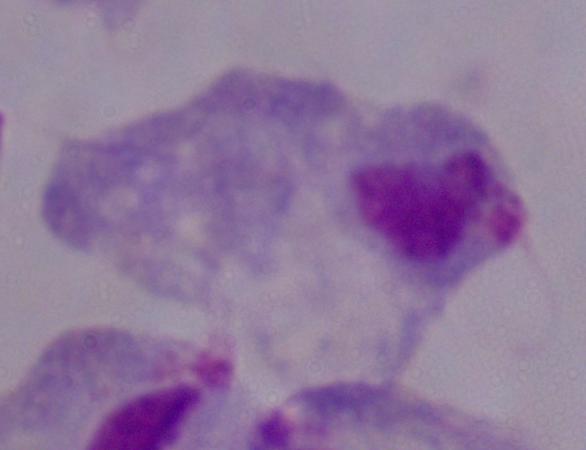
Captured at 1000x magnification. Photomicrograph. A trichomonad is shown.